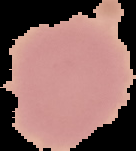
Summary:
  - Result: no Plasmodium parasites detected
  - Image size: 136×151 pixels
  - Image type: segmented cell region with the area outside set to black
  - Preparation: thin blood film